State which parasite is depicted.
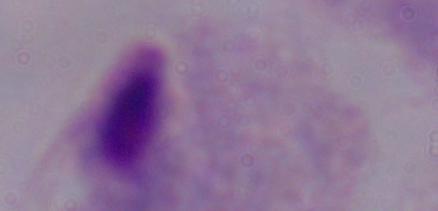

A trichomonad.

magnification: 1000x
modality: photomicrograph